Give the extent of all white blood cells.
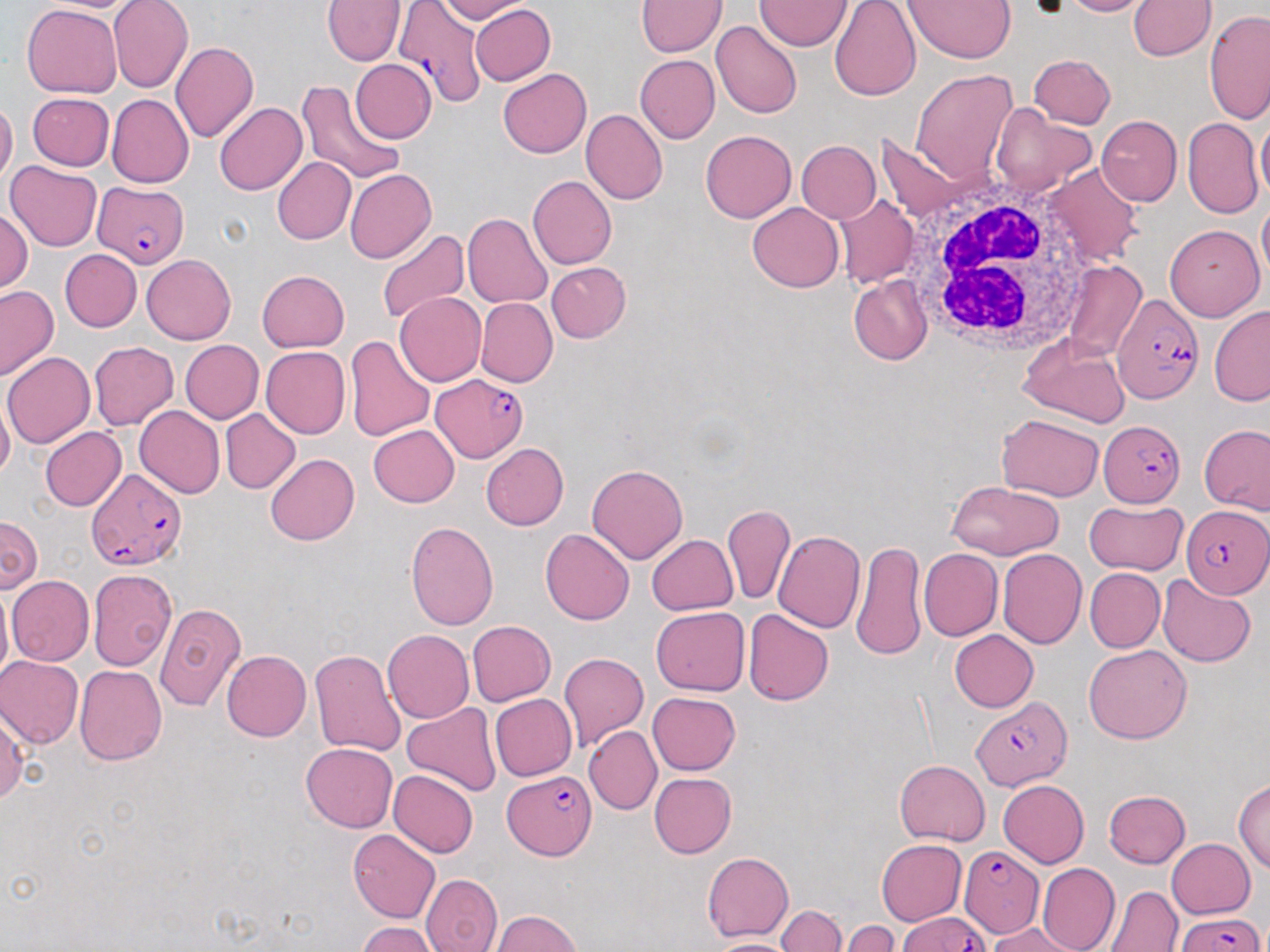

Approximate bounding boxes as (x1, y1, x2, y2) in pixels.
White blood cells: (1039, 164, 1145, 268), (903, 176, 1098, 356).

Plasmodium falciparum-infected red blood cell locations: (392, 0, 489, 105), (94, 180, 188, 269), (1112, 291, 1204, 404), (432, 374, 527, 461), (1098, 421, 1184, 506), (87, 467, 187, 571), (1181, 504, 1268, 598), (970, 695, 1071, 790), (503, 769, 594, 860), (959, 846, 1042, 938), (1176, 909, 1265, 952), (899, 910, 988, 952). Uninfected red blood cell locations: (322, 0, 406, 65), (435, 0, 531, 24), (638, 0, 727, 56), (829, 0, 921, 101), (904, 0, 1017, 63), (1059, 0, 1154, 17), (109, 1, 193, 93), (754, 1, 853, 51), (1129, 2, 1215, 61), (23, 4, 122, 97), (469, 4, 555, 85), (1204, 9, 1270, 126), (711, 20, 802, 119), (170, 41, 258, 143), (1029, 54, 1116, 128), (635, 55, 719, 144), (350, 59, 436, 142), (498, 68, 591, 158), (911, 69, 1019, 184), (296, 80, 405, 187), (27, 92, 114, 171), (106, 94, 193, 188), (0, 99, 17, 186), (214, 102, 308, 195), (990, 104, 1095, 198), (580, 108, 667, 204), (1096, 115, 1183, 206), (1255, 117, 1270, 203), (1182, 118, 1263, 219), (701, 130, 796, 223), (874, 134, 965, 225), (796, 141, 880, 223), (271, 157, 356, 245), (4, 161, 101, 252), (1041, 162, 1143, 268), (344, 169, 435, 264), (528, 175, 617, 270), (835, 194, 919, 289), (1257, 196, 1270, 286), (748, 202, 844, 292), (0, 209, 32, 293), (463, 212, 553, 308), (1164, 225, 1264, 322), (376, 229, 471, 325), (60, 249, 142, 332), (141, 253, 235, 343), (546, 261, 632, 343), (1060, 261, 1147, 361), (256, 270, 350, 353), (849, 274, 932, 366), (0, 286, 58, 380), (394, 292, 486, 386), (476, 297, 558, 387), (1209, 306, 1270, 407), (1017, 334, 1130, 426), (344, 335, 436, 442), (179, 340, 263, 424), (88, 341, 178, 431), (260, 346, 350, 439), (3, 352, 95, 447), (0, 394, 14, 483), (134, 405, 225, 497), (219, 409, 300, 493), (997, 413, 1105, 501), (1198, 424, 1269, 516), (369, 425, 460, 507), (41, 427, 126, 510), (480, 443, 569, 530), (265, 453, 359, 545), (587, 463, 688, 564), (948, 480, 1065, 559), (1084, 498, 1186, 574), (723, 505, 795, 606), (664, 510, 789, 631), (0, 514, 42, 594), (405, 522, 498, 630), (540, 528, 636, 624), (773, 530, 865, 633), (646, 534, 739, 615), (852, 539, 925, 661), (919, 548, 1002, 640), (997, 549, 1086, 649), (1084, 567, 1164, 652), (88, 569, 177, 672), (7, 575, 94, 666), (1157, 576, 1256, 667), (0, 581, 13, 690), (155, 603, 246, 711), (651, 606, 749, 696), (742, 609, 835, 706), (467, 620, 556, 705), (382, 630, 475, 723), (949, 630, 1038, 712), (1084, 644, 1192, 743), (221, 650, 312, 741), (309, 650, 407, 757), (559, 652, 648, 750), (0, 656, 84, 749), (74, 665, 167, 766), (647, 691, 742, 775), (489, 693, 577, 781), (403, 703, 502, 797), (0, 704, 27, 805), (584, 725, 662, 815), (301, 743, 397, 832), (894, 759, 990, 846), (388, 769, 478, 858), (649, 773, 736, 857), (1234, 778, 1270, 875), (997, 779, 1089, 866), (1103, 790, 1190, 868), (348, 829, 440, 923), (876, 839, 967, 926), (1166, 839, 1255, 918), (702, 852, 794, 942), (1036, 863, 1120, 952), (421, 873, 503, 952), (1105, 886, 1183, 952), (776, 905, 846, 952), (492, 910, 581, 951), (840, 921, 899, 952), (357, 922, 436, 952), (988, 923, 1088, 952), (704, 937, 804, 952). Slide-level diagnosis: Plasmodium falciparum. Single field of view. Image is 1270×952 pixels. May-Grünwald-Giemsa stain. Light microscopy. Thin blood film. Captured at 1000x magnification.